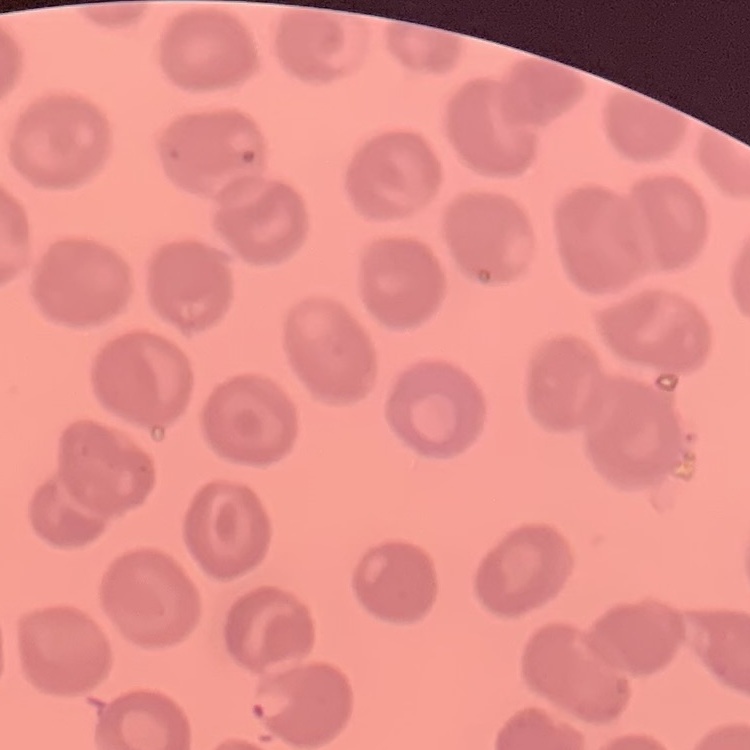

erythrocyte morphology = no rouleaux formation
stain = Field's or Giemsa
preparation = thin blood film
image type = one tile cut from a larger photomicrograph